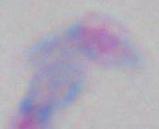

Summary:
  - Magnification: 1000x
  - Identification: Toxoplasma gondii
  - Modality: micrograph